Report the malaria status of this cell.
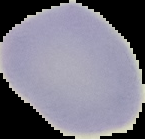

It is uninfected.

From a thin blood smear. Image is 145×139 pixels. Segmented cell region on a black background.